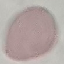

Malaria status: uninfected. Photographed with a smartphone camera at the microscope eyepiece. Thin smear of blood. Cell patch, automatically extracted from a larger field of view and resized to 64 × 64 pixels. Giemsa-stained preparation.